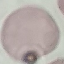

malaria_status: uninfected
capture: smartphone camera at the microscope eyepiece
image_type: cell patch, automatically extracted from a larger field of view and resized to 64 × 64 pixels
preparation: thin blood film
stain: Giemsa